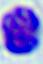

{
  "identification": "white blood cell",
  "modality": "micrograph",
  "magnification": "400x"
}